Classify this cell by malaria status.
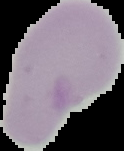

Uninfected.

image size = 124×151 pixels
image type = cell region segmented out of the field of view; surrounding area masked to black
preparation = thin blood film